Report the malaria status of this cell.
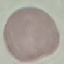

It is uninfected.

Summary:
  - Preparation: thin smear
  - Capture: smartphone through the microscope eyepiece
  - Stain: Giemsa
  - Image type: cell patch, automatically extracted from a larger field of view and resized to 64 × 64 pixels